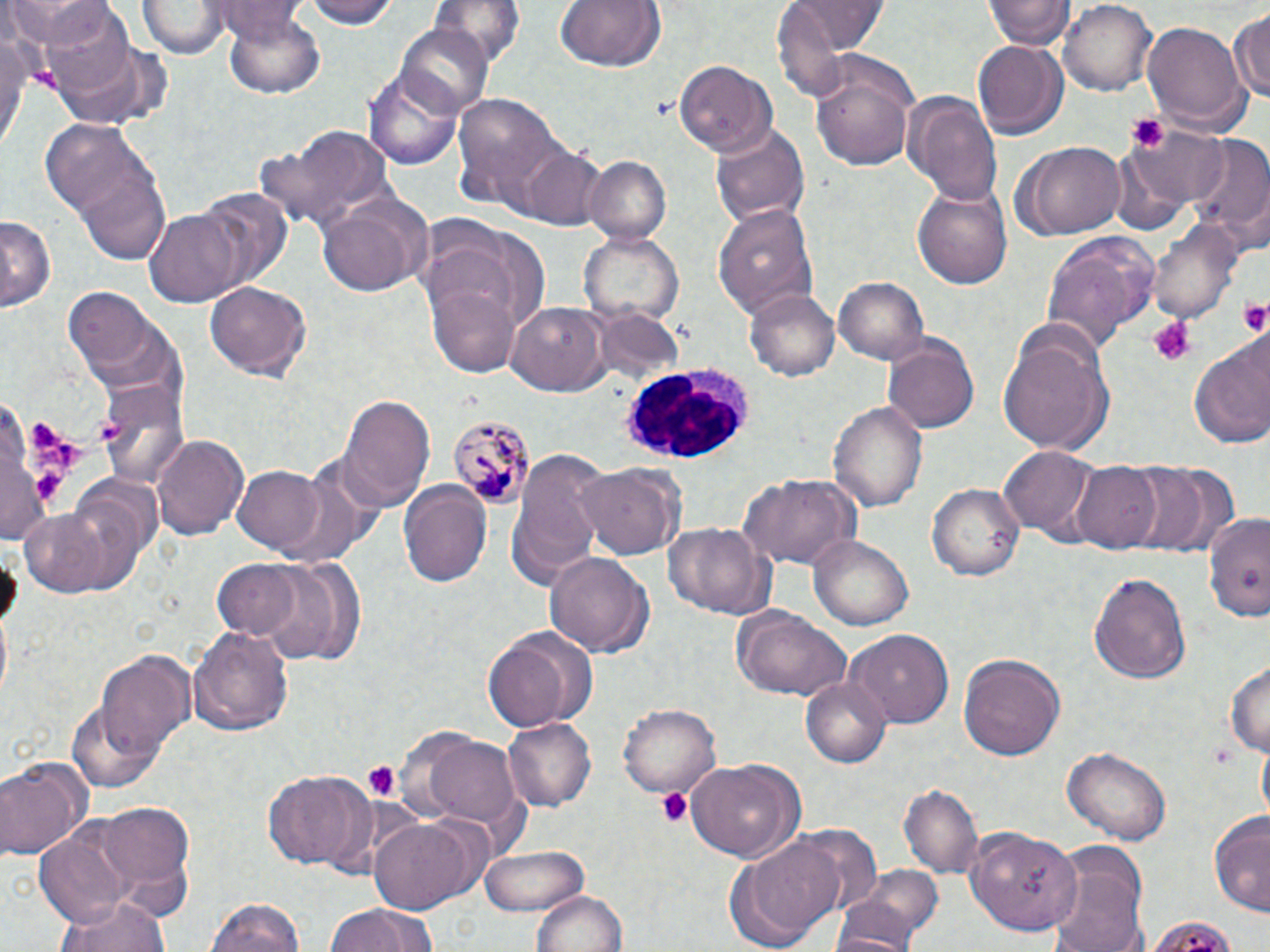

Summary:
  - Coordinate format: approximate bounding boxes as named x1/y1/x2/y2 corners in pixels
  - Uninfected red blood cell locations: (x1=7, y1=0, x2=108, y2=50), (x1=298, y1=0, x2=401, y2=30), (x1=427, y1=0, x2=526, y2=64), (x1=554, y1=0, x2=666, y2=75), (x1=988, y1=0, x2=1070, y2=49), (x1=140, y1=1, x2=228, y2=59), (x1=1059, y1=1, x2=1158, y2=96), (x1=214, y1=2, x2=305, y2=41), (x1=785, y1=2, x2=892, y2=52), (x1=41, y1=4, x2=136, y2=95), (x1=223, y1=6, x2=325, y2=97), (x1=1229, y1=8, x2=1270, y2=111), (x1=1141, y1=19, x2=1250, y2=135), (x1=398, y1=24, x2=492, y2=116), (x1=1, y1=26, x2=33, y2=154), (x1=974, y1=38, x2=1066, y2=139), (x1=808, y1=50, x2=922, y2=171), (x1=673, y1=59, x2=777, y2=158), (x1=365, y1=63, x2=466, y2=170), (x1=452, y1=91, x2=568, y2=206), (x1=901, y1=91, x2=1005, y2=206), (x1=41, y1=119, x2=174, y2=262), (x1=710, y1=122, x2=812, y2=227), (x1=1129, y1=123, x2=1229, y2=210), (x1=1184, y1=136, x2=1270, y2=253), (x1=1014, y1=141, x2=1128, y2=240), (x1=517, y1=146, x2=610, y2=230), (x1=583, y1=155, x2=672, y2=246), (x1=910, y1=185, x2=1014, y2=289), (x1=197, y1=188, x2=291, y2=288), (x1=317, y1=189, x2=431, y2=296), (x1=715, y1=207, x2=817, y2=320), (x1=146, y1=210, x2=243, y2=306), (x1=0, y1=214, x2=54, y2=313), (x1=422, y1=217, x2=549, y2=342), (x1=1149, y1=220, x2=1240, y2=324), (x1=577, y1=230, x2=684, y2=327), (x1=1042, y1=234, x2=1158, y2=353), (x1=834, y1=276, x2=930, y2=365), (x1=426, y1=279, x2=521, y2=377), (x1=206, y1=280, x2=309, y2=381), (x1=62, y1=289, x2=177, y2=390), (x1=747, y1=290, x2=839, y2=381), (x1=507, y1=303, x2=609, y2=395), (x1=595, y1=309, x2=684, y2=382), (x1=995, y1=324, x2=1113, y2=455), (x1=1189, y1=331, x2=1270, y2=452), (x1=883, y1=336, x2=978, y2=434), (x1=101, y1=378, x2=191, y2=490), (x1=339, y1=393, x2=435, y2=506), (x1=829, y1=397, x2=927, y2=515), (x1=152, y1=433, x2=248, y2=541), (x1=1000, y1=447, x2=1096, y2=541), (x1=508, y1=448, x2=612, y2=589), (x1=1121, y1=461, x2=1214, y2=553), (x1=266, y1=463, x2=380, y2=573), (x1=579, y1=463, x2=682, y2=561), (x1=1072, y1=463, x2=1162, y2=552), (x1=233, y1=466, x2=324, y2=552), (x1=739, y1=474, x2=859, y2=573), (x1=397, y1=477, x2=493, y2=586), (x1=930, y1=483, x2=1024, y2=581), (x1=16, y1=505, x2=119, y2=596), (x1=1203, y1=513, x2=1270, y2=625), (x1=663, y1=522, x2=773, y2=619), (x1=809, y1=535, x2=914, y2=632), (x1=544, y1=549, x2=651, y2=655), (x1=252, y1=555, x2=361, y2=667), (x1=207, y1=556, x2=314, y2=646), (x1=1087, y1=570, x2=1191, y2=684), (x1=731, y1=607, x2=849, y2=702), (x1=190, y1=625, x2=294, y2=736), (x1=482, y1=628, x2=592, y2=730), (x1=847, y1=630, x2=952, y2=728), (x1=95, y1=650, x2=196, y2=763), (x1=958, y1=654, x2=1065, y2=763), (x1=1225, y1=659, x2=1269, y2=760), (x1=802, y1=675, x2=891, y2=769), (x1=67, y1=703, x2=164, y2=793), (x1=619, y1=704, x2=721, y2=799), (x1=504, y1=717, x2=595, y2=812), (x1=418, y1=729, x2=526, y2=831), (x1=1061, y1=744, x2=1172, y2=844), (x1=0, y1=756, x2=91, y2=862), (x1=686, y1=758, x2=804, y2=862), (x1=263, y1=767, x2=377, y2=872), (x1=901, y1=783, x2=982, y2=878), (x1=80, y1=801, x2=199, y2=915), (x1=1209, y1=813, x2=1270, y2=915), (x1=367, y1=816, x2=480, y2=916), (x1=790, y1=825, x2=882, y2=917), (x1=966, y1=828, x2=1080, y2=935), (x1=34, y1=829, x2=135, y2=931), (x1=728, y1=834, x2=844, y2=948), (x1=1047, y1=841, x2=1150, y2=952), (x1=479, y1=844, x2=588, y2=917), (x1=829, y1=881, x2=933, y2=952), (x1=528, y1=888, x2=629, y2=952), (x1=53, y1=893, x2=170, y2=952), (x1=205, y1=896, x2=309, y2=952), (x1=323, y1=901, x2=440, y2=952)
  - Platelet locations: (x1=1123, y1=113, x2=1168, y2=155), (x1=1237, y1=297, x2=1270, y2=336), (x1=1147, y1=317, x2=1193, y2=366), (x1=28, y1=416, x2=81, y2=469), (x1=95, y1=419, x2=124, y2=446), (x1=34, y1=472, x2=63, y2=499), (x1=1208, y1=739, x2=1237, y2=769), (x1=360, y1=760, x2=402, y2=801), (x1=656, y1=787, x2=691, y2=828)
  - Plasmodium malariae-infected red blood cell locations: (x1=447, y1=413, x2=531, y2=511)
  - White blood cell locations: (x1=622, y1=365, x2=758, y2=462)
  - Slide-level diagnosis: Plasmodium malariae
  - Magnification: 1000x
  - Stain: May-Grünwald-Giemsa
  - Modality: optical microscopy
  - Preparation: thin blood film
  - Image size: 1270×952 pixels
  - Field of view: one of a larger specimen